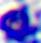

A leukocyte is shown. 400x magnification. Photomicrograph.